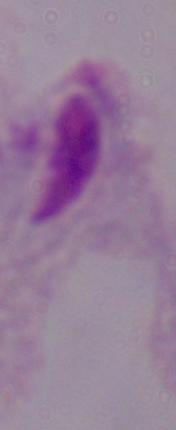
Captured at 1000x magnification. Photomicrograph. A trichomonad is seen.